Locate every blood parasite and identify its species.
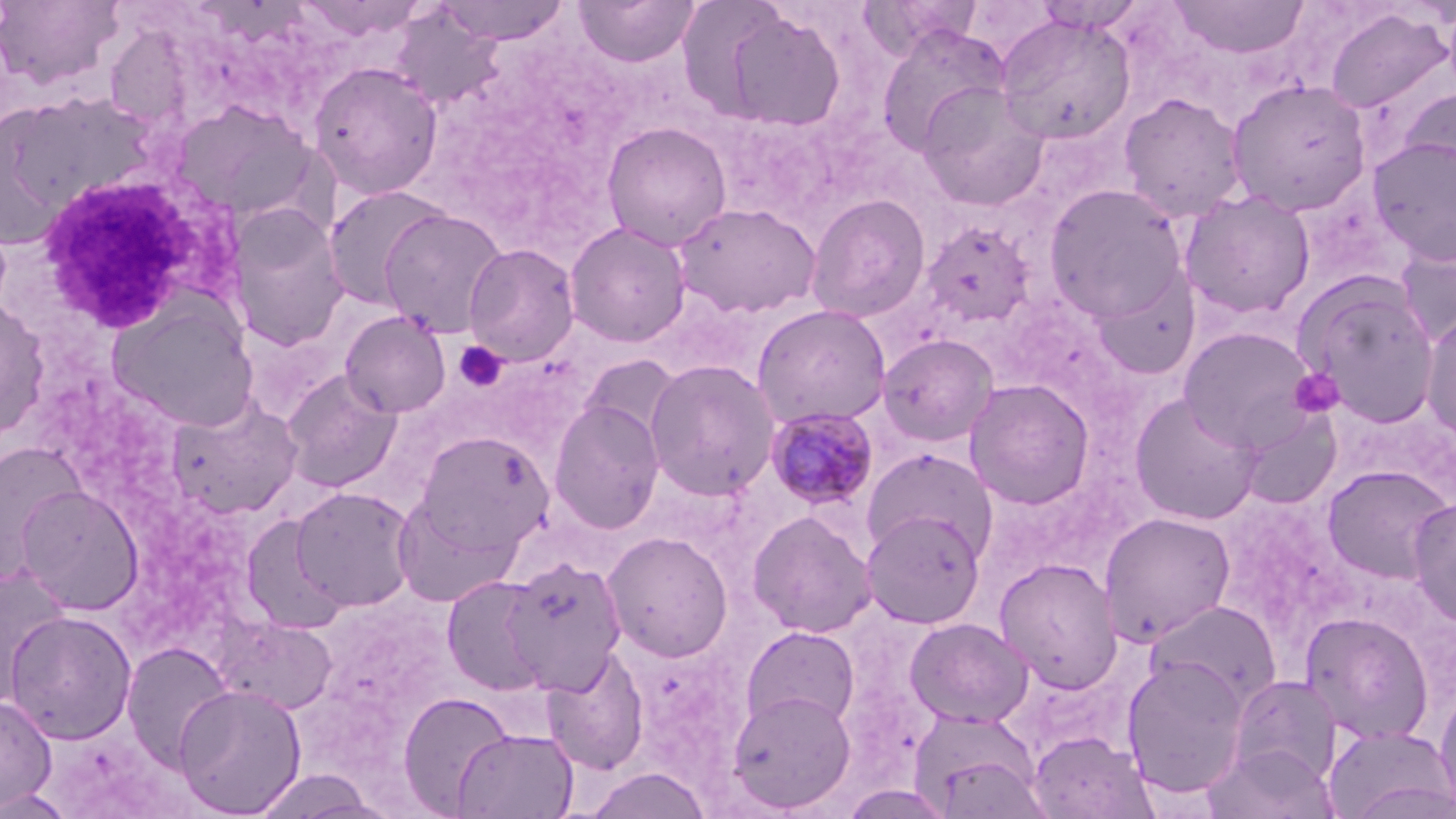
Approximate bounding boxes as (x1,y1)-(x2,y2) corner pairs in pixels.
Plasmodium malariae-infected red blood cells: (765,406)-(880,511).
No Plasmodium falciparum, Plasmodium ovale, Plasmodium vivax, Babesia divergens, or Trypanosoma brucei observed.

White blood cell locations: (33,169)-(233,334). Uninfected red blood cell locations: (0,0)-(127,91), (293,0)-(428,42), (573,0)-(700,68), (857,0)-(982,59), (1169,0)-(1309,59), (434,1)-(572,45), (710,5)-(847,132), (390,7)-(508,111), (1324,8)-(1453,116), (994,12)-(1137,147), (874,24)-(1010,157), (105,26)-(195,130), (308,61)-(444,200), (1226,79)-(1372,217), (916,83)-(1049,211), (1399,85)-(1456,198), (1118,93)-(1247,223), (167,99)-(322,226), (601,121)-(732,250), (1367,136)-(1456,265), (1042,183)-(1191,324), (322,185)-(452,310), (1179,189)-(1316,320), (805,193)-(931,323), (672,202)-(820,318), (224,203)-(350,351), (379,208)-(508,338), (920,220)-(1035,330), (564,221)-(691,347), (1396,230)-(1456,346), (463,242)-(580,366), (1298,279)-(1440,428), (0,298)-(51,440), (108,298)-(259,431), (751,303)-(892,429), (1422,310)-(1456,444), (340,311)-(450,417), (1179,326)-(1319,451), (877,333)-(1000,447), (580,353)-(685,448), (643,359)-(781,500), (281,370)-(402,492), (963,378)-(1096,509), (1128,392)-(1263,526), (166,396)-(302,519), (549,399)-(665,534), (1235,405)-(1345,510), (416,431)-(552,553), (0,442)-(87,581), (862,446)-(997,562), (1322,464)-(1454,584), (17,484)-(144,615), (290,485)-(418,612), (392,495)-(518,608), (1407,498)-(1456,627), (239,510)-(353,637), (747,510)-(877,638), (861,510)-(985,628), (1098,511)-(1236,645), (602,531)-(734,663), (501,555)-(627,692), (994,557)-(1124,694), (1,563)-(73,708), (441,575)-(551,696), (1145,600)-(1282,711), (4,610)-(138,744), (1299,611)-(1435,744), (904,617)-(1033,728), (221,618)-(338,715), (740,625)-(860,732), (121,640)-(235,772), (542,648)-(650,774), (1120,655)-(1251,798), (1228,674)-(1342,787), (172,682)-(307,817), (1434,682)-(1456,817), (727,690)-(857,813), (397,692)-(516,815), (0,695)-(56,810), (909,708)-(1046,816), (1323,724)-(1455,819), (453,727)-(578,819), (1027,731)-(1157,818), (1204,742)-(1338,819), (583,767)-(712,819), (249,769)-(384,818), (0,789)-(78,819). Platelet locations: (454,341)-(508,393), (1289,368)-(1344,418). Slide-level diagnosis: Plasmodium malariae. Image is 1456×819 pixels. Thin blood film. Optical microscopy. 1000x magnification. May-Grünwald-Giemsa stain. One field of a larger specimen.